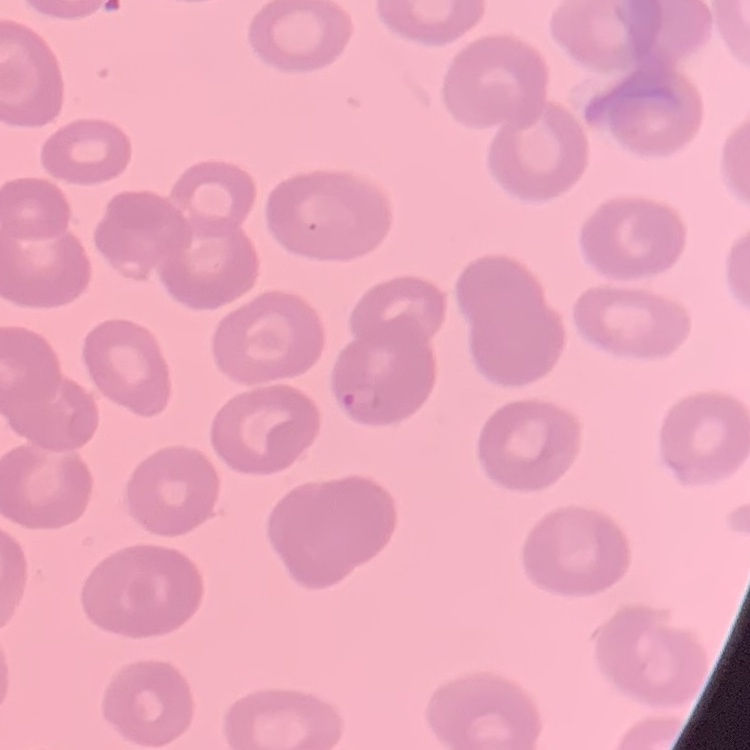

Summary:
  - Erythrocyte morphology: no rouleaux formation
  - Stain: Field's or Giemsa
  - Image type: one tile cut from a larger photomicrograph
  - Preparation: thin peripheral smear